Classify this cell by malaria status.
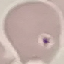
Uninfected.

Photographed with a smartphone camera at the microscope eyepiece. Cell patch, automatically extracted from a larger field of view and resized to 64 × 64 pixels. Giemsa-stained preparation. Thin blood film.